Classify this cell by malaria status.
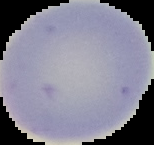

It is uninfected.

preparation = thin blood film
image type = segmented cell region with the area outside set to black
image size = 154×145 pixels